Draw a bounding box around every malaria parasite.
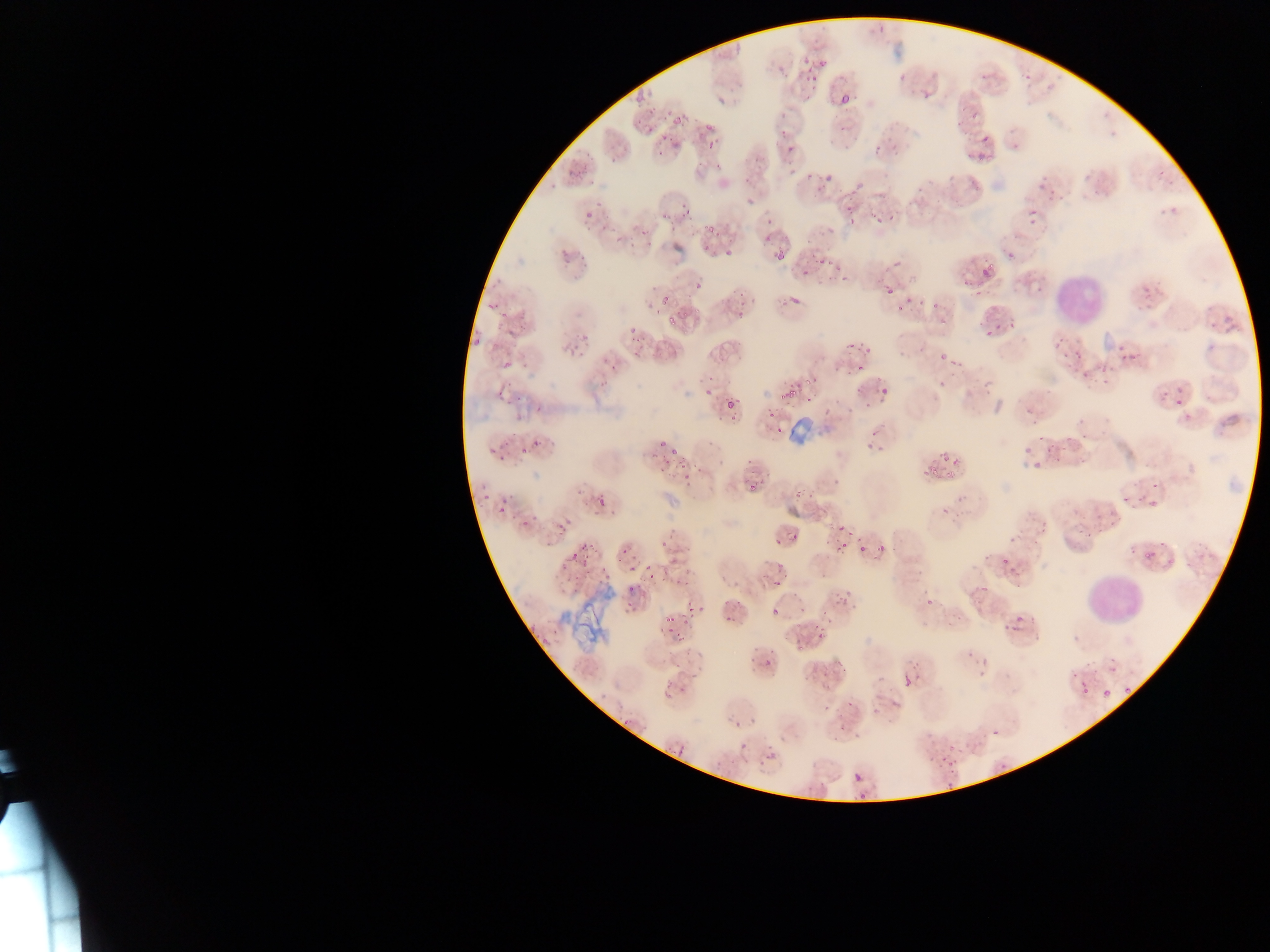

Approximate bounding boxes as [left, top, right, bottom] in pixels.
Malaria parasites: [801, 47, 814, 69], [780, 63, 798, 83], [804, 66, 824, 85], [889, 73, 907, 83], [1018, 74, 1035, 88], [915, 85, 942, 104], [833, 90, 848, 104], [671, 108, 686, 127], [628, 116, 655, 137], [692, 119, 718, 147], [833, 119, 848, 132], [983, 127, 1004, 149], [774, 128, 783, 137], [785, 139, 797, 153], [663, 141, 679, 153], [970, 143, 994, 159], [868, 151, 879, 163], [820, 171, 837, 188], [1034, 180, 1046, 188], [960, 183, 987, 193], [1047, 184, 1065, 203], [840, 190, 857, 212], [869, 206, 889, 224], [1022, 207, 1040, 225], [760, 218, 780, 234], [844, 218, 850, 226], [813, 249, 837, 266], [770, 254, 788, 265], [799, 255, 818, 280], [975, 262, 990, 276], [956, 264, 970, 285], [834, 267, 858, 280], [876, 277, 897, 299], [926, 288, 956, 310], [655, 290, 677, 308], [891, 291, 913, 309], [780, 295, 806, 313], [985, 324, 999, 340], [566, 335, 589, 356], [844, 337, 862, 350], [1049, 338, 1067, 352], [608, 341, 624, 352], [1111, 344, 1137, 378], [496, 348, 520, 377], [935, 352, 948, 362], [1070, 352, 1084, 369], [1079, 358, 1105, 382], [855, 362, 867, 375], [799, 364, 817, 386], [930, 368, 956, 391], [777, 380, 795, 395], [866, 383, 886, 402], [701, 386, 715, 398], [1154, 388, 1168, 410], [724, 397, 734, 409], [1173, 397, 1184, 412], [768, 411, 777, 420], [657, 439, 667, 448], [861, 445, 872, 455], [1020, 445, 1033, 464], [660, 448, 682, 469], [938, 448, 959, 463], [923, 457, 941, 476], [683, 464, 700, 478], [746, 481, 759, 495], [497, 486, 516, 516], [591, 490, 603, 512], [1120, 497, 1134, 507], [539, 514, 572, 550], [1096, 516, 1114, 524], [833, 519, 850, 540], [1002, 525, 1020, 544], [788, 533, 800, 543], [1070, 535, 1086, 547], [769, 536, 779, 546], [609, 537, 635, 556], [854, 541, 868, 555], [568, 542, 583, 563], [832, 542, 844, 556], [875, 545, 885, 559], [998, 557, 1012, 575], [657, 562, 683, 592], [627, 566, 636, 574], [564, 567, 578, 583], [595, 568, 605, 575], [771, 568, 785, 585], [833, 589, 849, 612], [919, 593, 936, 603], [620, 603, 636, 616], [697, 605, 707, 616], [771, 607, 781, 618], [723, 608, 740, 622], [999, 609, 1022, 635], [660, 612, 678, 622], [665, 624, 676, 633], [678, 624, 695, 650], [815, 624, 829, 644], [792, 636, 804, 652], [961, 647, 971, 661], [745, 648, 757, 657], [763, 656, 773, 670], [808, 656, 828, 681], [829, 662, 843, 676], [896, 672, 915, 686], [1074, 680, 1092, 698], [1097, 681, 1121, 697], [663, 683, 675, 694], [678, 683, 695, 697], [840, 695, 858, 717], [732, 719, 743, 730], [829, 722, 839, 736], [734, 741, 749, 759], [938, 741, 960, 768], [852, 771, 866, 787].

Leukocyte locations: [1051, 264, 1109, 328], [1080, 566, 1150, 630]. Image is 1270×952 pixels. Photographed through a microscope with a mobile-phone camera. Thin blood film. One field of view. Collected in Ghana.